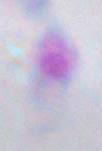

{
  "identification": "Toxoplasma gondii",
  "modality": "micrograph",
  "magnification": "1000x"
}